Draw a bounding box around every leukocyte (white blood cell).
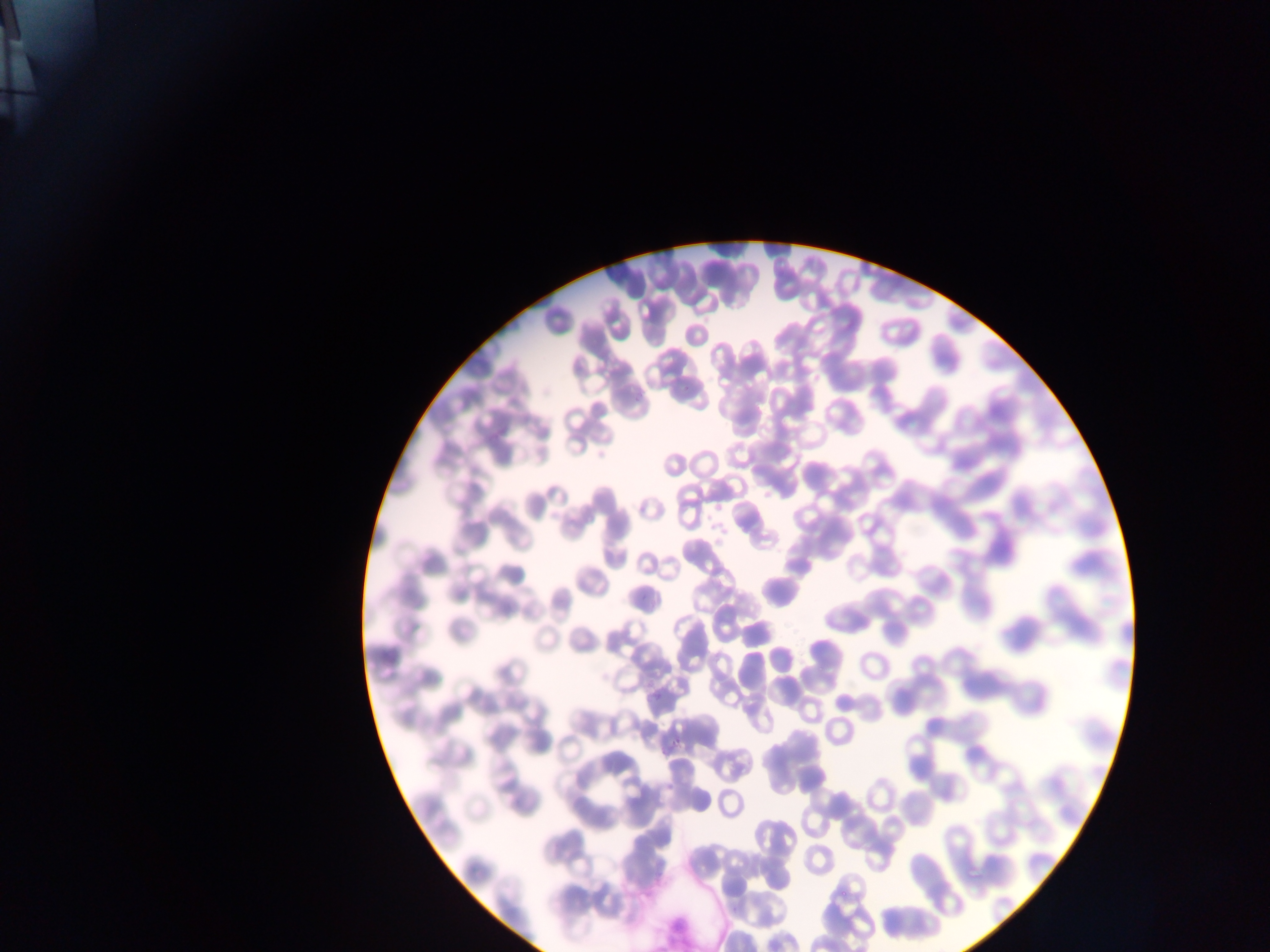

No leukocytes observed.

Plasmodium parasite locations = approximate bounding boxes as (left, top, right, bottom) in pixels: (651, 690, 662, 701), (670, 737, 686, 745)
preparation = thin blood film
capture = mobile-phone photograph through a microscope
image size = 1270×952 pixels
field of view = single
country = Ghana